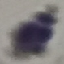
malaria status = uninfected
preparation = thin blood smear
capture = smartphone through the microscope eyepiece
image type = automatically extracted cell patch, resized to 64 × 64 pixels
stain = Giemsa